Assess this cell for malaria.
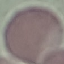
Uninfected.

Summary:
  - Capture: smartphone camera at the microscope eyepiece
  - Image type: cell patch, automatically extracted from a larger field of view and resized to 64 × 64 pixels
  - Preparation: thin smear
  - Stain: Giemsa